Assess this cell for malaria.
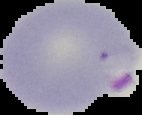
Parasitized.

Summary:
  - Preparation: thin blood film
  - Image type: segmented cell region on a black background
  - Image size: 142×115 pixels